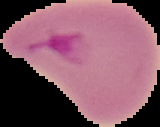 Image is 160×127 pixels. Segmented cell region on a black background. Malaria status: parasitized. From a thin blood film.